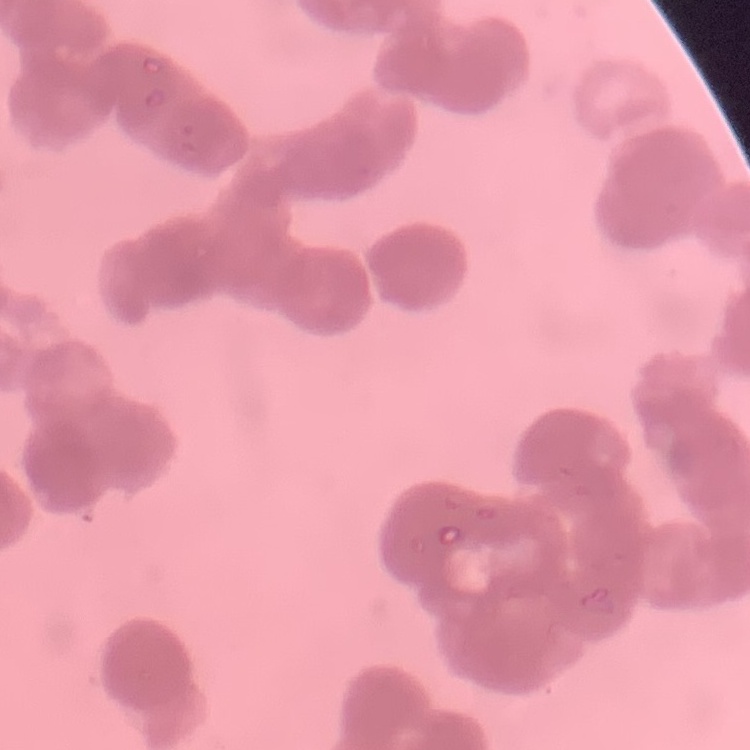 The red blood cells exhibit rouleaux formation. One tile cut from a larger photomicrograph. Stained with either Field's or Giemsa. Thin peripheral smear.